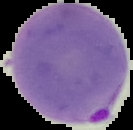
Summary:
  - Malaria status: parasitized
  - Preparation: thin blood smear
  - Image type: cell region segmented out of the field of view; surrounding area masked to black
  - Image size: 133×130 pixels